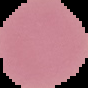
preparation = thin blood smear
malaria status = uninfected
image type = segmented cell region on a black background
image size = 88×88 pixels